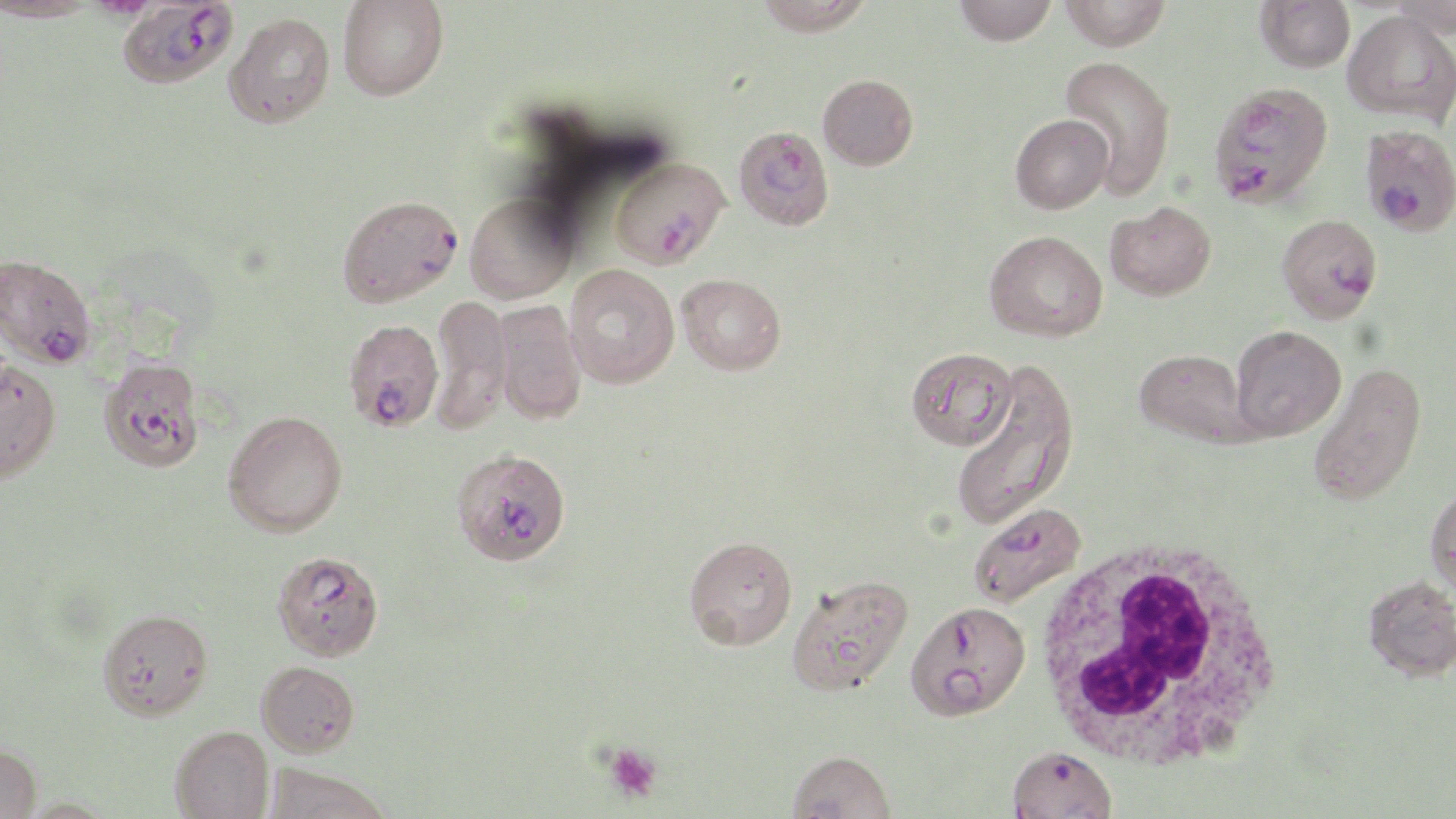

Approximate bounding boxes as (x1,y1)-(x2,y2) corner pairs in pixels. Uninfected red blood cell locations: (338,0)-(448,100), (755,0)-(873,35), (954,0)-(1057,45), (1060,0)-(1171,51), (1256,0)-(1355,72), (1390,0)-(1456,37), (1343,10)-(1455,125), (223,12)-(335,128), (1059,55)-(1176,198), (818,74)-(918,170), (1010,113)-(1113,214), (464,191)-(578,304), (1105,201)-(1216,300), (984,230)-(1108,342), (564,264)-(680,388), (677,273)-(786,375), (429,293)-(512,434), (494,301)-(587,424), (1230,325)-(1346,440), (906,346)-(1018,450), (1134,348)-(1248,444), (0,358)-(61,484), (1307,360)-(1427,507), (950,362)-(1079,531), (223,409)-(347,537), (1426,485)-(1456,599), (683,535)-(797,649), (787,573)-(913,696), (1363,575)-(1456,681), (98,608)-(213,720), (256,661)-(360,757), (170,725)-(274,819), (0,742)-(41,819), (788,750)-(896,818), (263,762)-(394,819). White blood cell locations: (1031,539)-(1286,770). Plasmodium falciparum-infected red blood cell locations: (117,0)-(239,90), (1207,81)-(1334,209), (1359,123)-(1456,236), (733,124)-(834,231), (611,157)-(730,269), (337,194)-(462,307), (1277,213)-(1383,322), (1,253)-(97,369), (344,319)-(443,432), (99,356)-(205,473), (452,452)-(572,569), (969,501)-(1087,608), (273,560)-(381,660), (905,600)-(1031,721), (1007,744)-(1117,818). Platelet locations: (603,742)-(663,804). Slide-level diagnosis: Plasmodium falciparum. Image is 1456×819 pixels. Thin blood film. One field of a larger specimen. 1000x magnification. May-Grünwald-Giemsa stain. Optical microscopy.